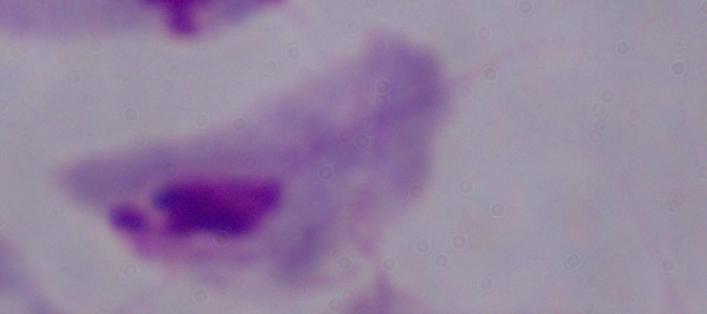
identification: trichomonad
magnification: 1000x
modality: micrograph